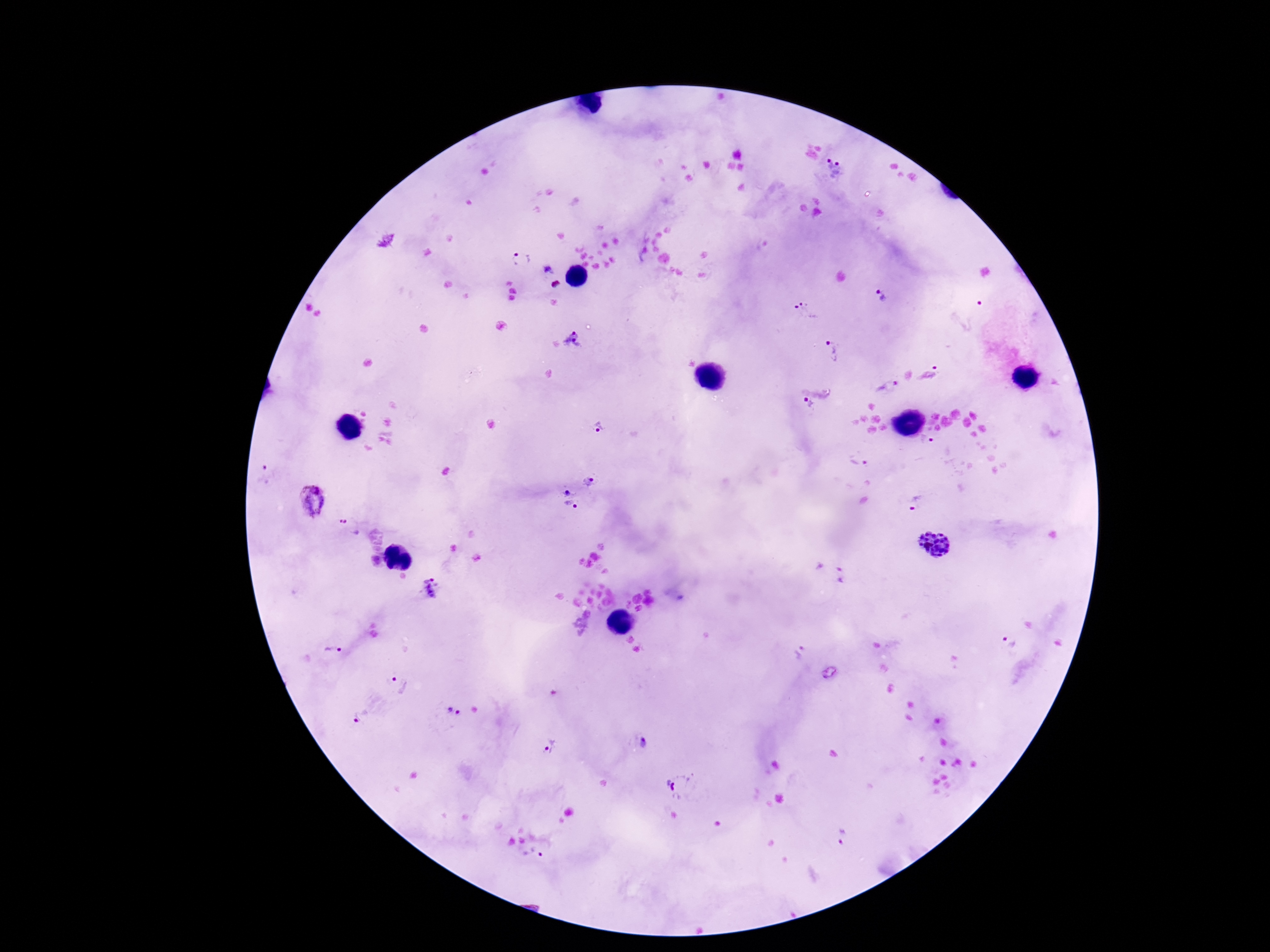

Approximate centers as (x, y) in pixels. Plasmodium parasite locations: (835, 169), (521, 260), (548, 269), (558, 284), (879, 296), (806, 312), (576, 340), (833, 352), (930, 372), (887, 386), (808, 405), (598, 428), (927, 441), (859, 461), (264, 475), (590, 481), (567, 491), (312, 500), (918, 504), (571, 507), (350, 526), (934, 545), (432, 587), (1008, 642), (335, 653), (799, 656), (400, 683), (453, 711), (359, 718), (645, 743), (551, 747), (680, 786), (844, 836), (533, 855). Thick blood film. Patient malaria status: infected. Giemsa stain. 100x magnification. Smartphone photograph taken through the microscope eyepiece. Single field of view. Image is 1270×952 pixels.